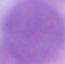
modality = photomicrograph
magnification = 1000x
identification = red blood cell